Identify the preparation type.
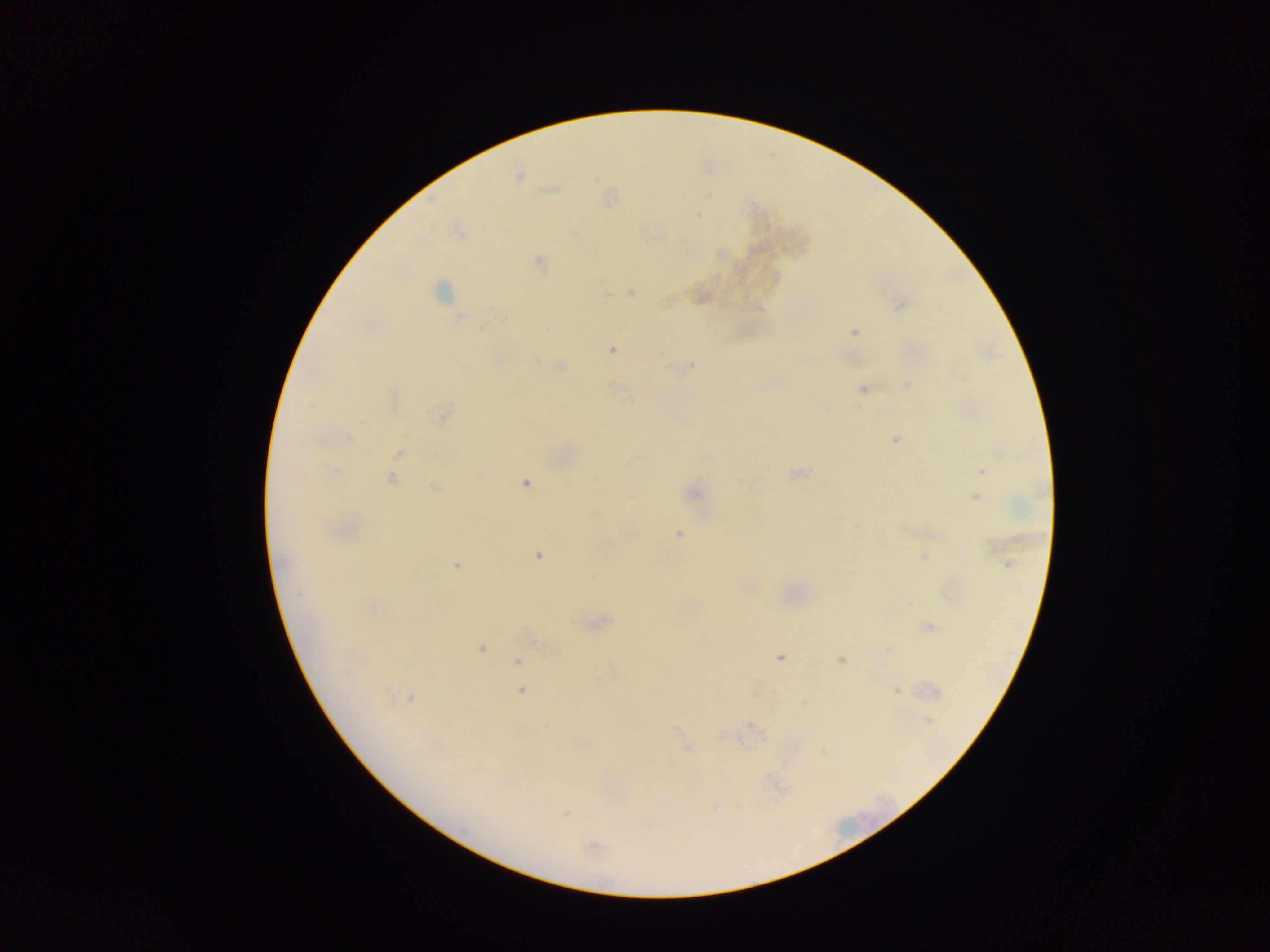

This is a thick smear.

malaria parasite locations = approximate centers as {x, y} in pixels: {519, 175}, {698, 213}, {539, 261}, {440, 291}, {631, 293}, {606, 294}, {900, 304}, {459, 317}, {854, 331}, {612, 349}, {691, 365}, {559, 366}, {908, 384}, {616, 387}, {863, 389}, {310, 406}, {443, 414}, {348, 438}, {896, 439}, {400, 453}, {982, 470}, {335, 471}, {799, 473}, {598, 476}, {393, 480}, {525, 483}, {435, 487}, {694, 492}, {975, 497}, {347, 529}, {678, 533}, {538, 556}, {924, 557}, {1008, 564}, {456, 565}, {298, 593}, {928, 627}, {480, 648}, {780, 658}, {842, 660}, {517, 661}, {347, 670}, {521, 691}, {897, 691}, {388, 698}, {412, 698}, {928, 720}, {547, 726}, {754, 727}, {687, 748}, {567, 814}, {595, 846}
image size = 1270×952 pixels
capture = mobile-phone photograph through a microscope
country = Ghana
field of view = single